Point out each malaria parasite.
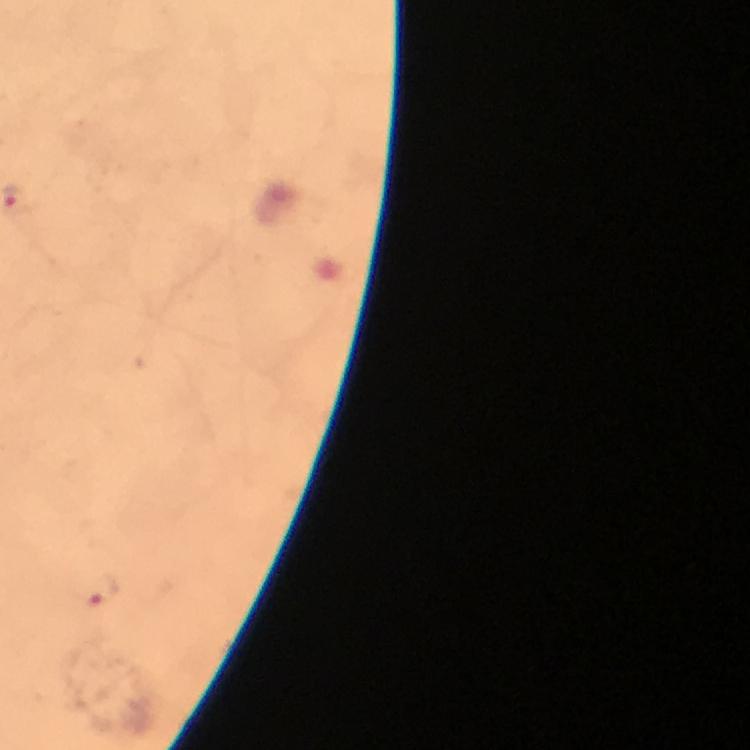

Approximate centers as {x, y} in pixels.
Malaria parasites: {101, 592}.

Summary:
  - Preparation: thick blood film
  - Stain: Giemsa
  - Context: from a malaria diagnostic workup
  - Immersion oil: used
  - Cropped from: one field of view
  - Capture: smartphone camera through the microscope
  - Magnification: 100x
  - Image size: 750×750 pixels